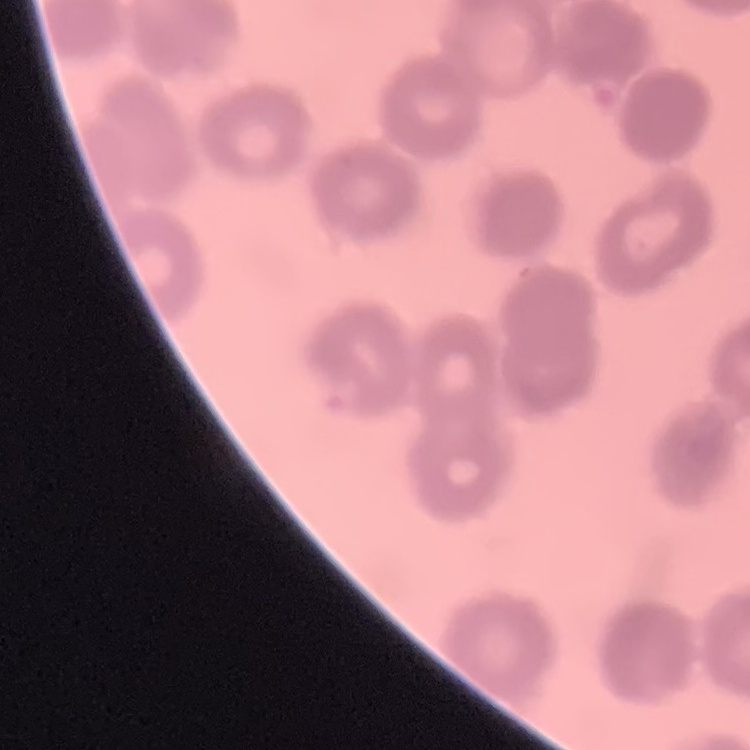
red blood cell morphology = rouleaux formation
stain = Field's or Giemsa
image type = square crop of a larger photomicrograph
preparation = thin blood film